Report the malaria status of this cell.
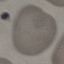
It is uninfected.

{
  "image_type": "automatically extracted cell patch, resized to 64 × 64 pixels",
  "stain": "Giemsa",
  "capture": "smartphone through the microscope eyepiece",
  "preparation": "thin blood smear"
}